Outline platelets.
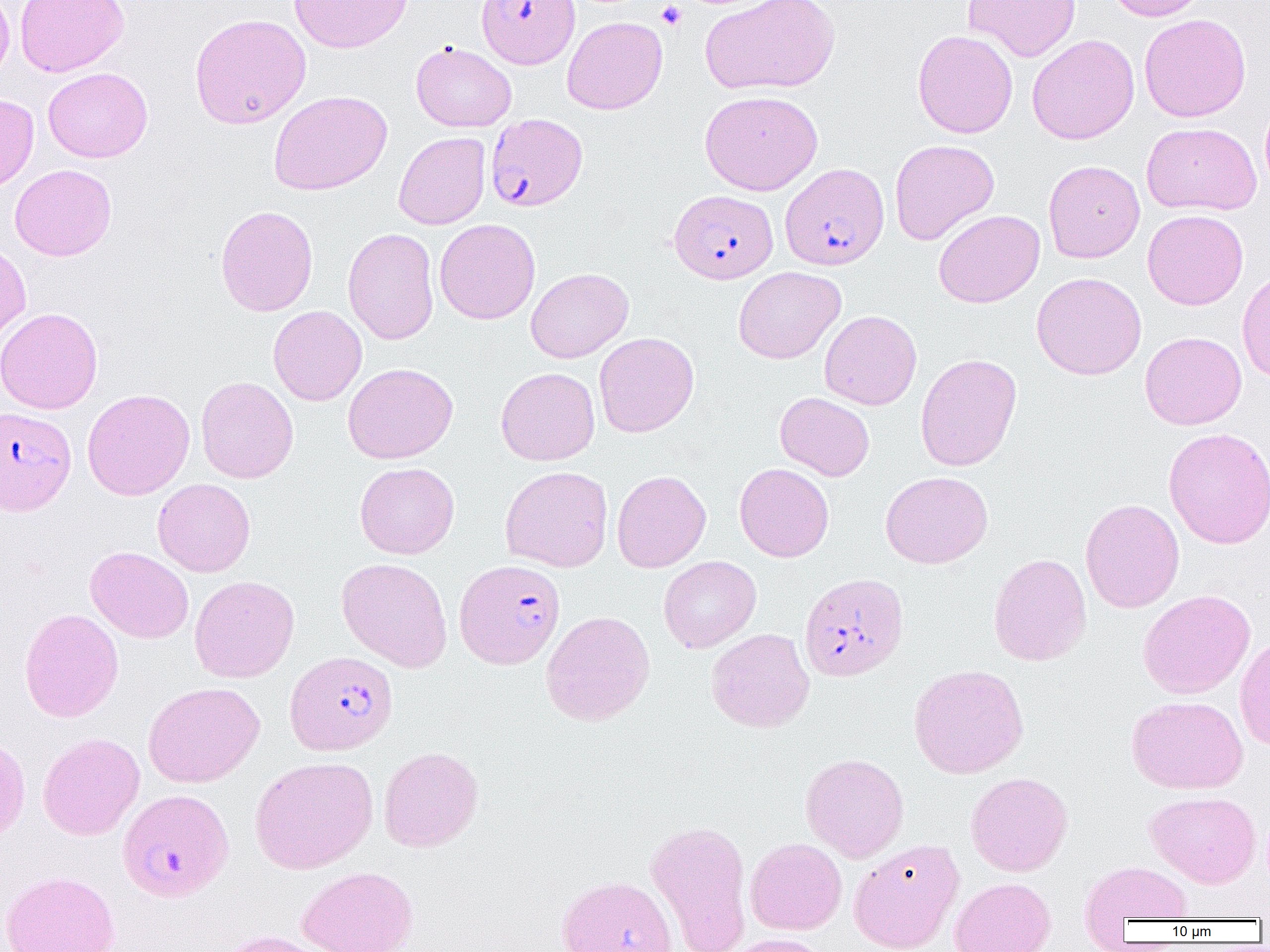
Approximate bounding boxes as [x1, y1, x2, y2] in pixels.
Platelets: [656, 1, 687, 30].

Summary:
  - Uninfected red blood cell locations: [0, 0, 15, 86], [14, 0, 129, 77], [288, 0, 412, 53], [700, 0, 840, 95], [963, 0, 1081, 62], [1105, 0, 1211, 21], [189, 13, 311, 129], [1139, 13, 1251, 122], [562, 16, 667, 114], [912, 29, 1018, 138], [1027, 34, 1139, 145], [411, 41, 517, 132], [43, 67, 153, 162], [268, 90, 392, 196], [700, 90, 823, 195], [0, 94, 39, 191], [1260, 96, 1270, 200], [1142, 122, 1262, 215], [393, 132, 490, 230], [889, 139, 999, 245], [1043, 159, 1145, 263], [10, 164, 116, 261], [215, 204, 318, 316], [933, 209, 1045, 308], [1142, 209, 1248, 310], [434, 218, 540, 324], [342, 228, 439, 345], [0, 239, 31, 345], [733, 266, 846, 364], [526, 268, 633, 362], [1237, 269, 1270, 382], [1031, 272, 1147, 380], [268, 305, 367, 406], [0, 307, 103, 415], [819, 310, 921, 410], [1140, 331, 1247, 429], [594, 332, 699, 437], [915, 353, 1022, 471], [343, 362, 458, 464], [495, 367, 600, 466], [196, 376, 298, 483], [82, 388, 195, 500], [775, 392, 875, 481], [1164, 426, 1270, 549], [354, 462, 459, 559], [734, 463, 834, 562], [500, 465, 613, 572], [611, 470, 711, 573], [880, 471, 993, 569], [153, 478, 255, 577], [1080, 499, 1185, 613], [85, 546, 194, 644], [988, 552, 1091, 666], [658, 555, 761, 653], [336, 557, 453, 673], [189, 575, 300, 683], [1137, 589, 1255, 699], [19, 608, 123, 722], [541, 610, 655, 726], [706, 628, 814, 732], [1235, 632, 1270, 751], [908, 664, 1029, 778], [143, 681, 264, 788], [1126, 695, 1248, 794], [38, 732, 145, 841], [0, 733, 31, 843], [378, 746, 484, 852], [800, 753, 909, 862], [250, 756, 378, 873], [965, 772, 1073, 877], [1146, 790, 1262, 887], [645, 819, 753, 952], [745, 837, 847, 935], [848, 838, 964, 952], [1080, 861, 1193, 925], [298, 866, 419, 952], [1, 870, 120, 952], [556, 874, 678, 952], [950, 877, 1056, 952], [211, 930, 334, 952], [720, 933, 830, 952]
  - Plasmodium falciparum-infected red blood cell locations: [477, 0, 579, 68], [486, 112, 587, 212], [780, 163, 889, 270], [669, 189, 778, 283], [1, 406, 76, 515], [454, 559, 566, 669], [799, 572, 909, 682], [285, 651, 398, 755], [118, 788, 234, 901]
  - Slide-level diagnosis: Plasmodium falciparum
  - Modality: optical microscopy
  - Image size: 1270×952 pixels
  - Preparation: thin blood film
  - Magnification: 1000x
  - Field of view: one of a larger specimen